Give the position of every Plasmodium parasite.
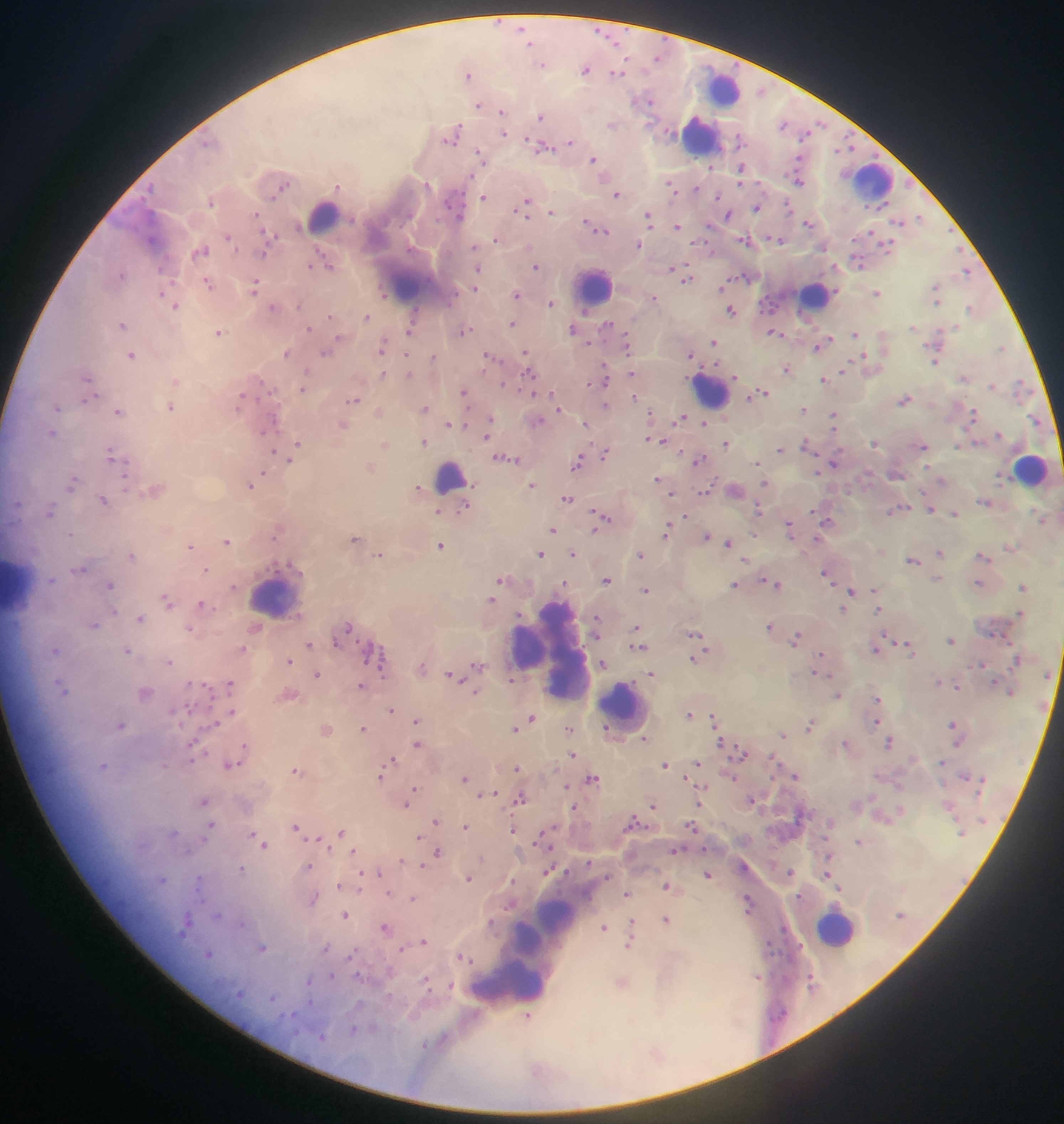
Approximate centers as {x, y} in pixels.
Plasmodium parasites: {497, 21}, {522, 28}, {598, 30}, {608, 36}, {531, 45}, {618, 45}, {625, 59}, {543, 65}, {585, 72}, {613, 73}, {624, 73}, {467, 75}, {650, 103}, {477, 105}, {500, 111}, {541, 118}, {821, 122}, {460, 124}, {784, 126}, {667, 130}, {506, 134}, {739, 134}, {459, 135}, {805, 135}, {526, 139}, {445, 140}, {570, 140}, {542, 141}, {455, 144}, {852, 148}, {551, 149}, {738, 149}, {836, 151}, {479, 152}, {536, 152}, {696, 157}, {798, 157}, {594, 159}, {486, 164}, {740, 164}, {710, 168}, {472, 175}, {668, 182}, {799, 182}, {427, 184}, {741, 184}, {290, 185}, {698, 189}, {281, 190}, {464, 192}, {676, 193}, {618, 195}, {274, 198}, {483, 198}, {445, 201}, {718, 201}, {789, 201}, {527, 202}, {465, 205}, {211, 206}, {449, 207}, {755, 209}, {516, 210}, {552, 211}, {791, 211}, {648, 212}, {257, 214}, {728, 216}, {459, 217}, {528, 217}, {438, 218}, {586, 220}, {810, 224}, {710, 225}, {651, 227}, {678, 228}, {263, 230}, {871, 230}, {595, 232}, {607, 232}, {276, 235}, {749, 236}, {768, 236}, {228, 237}, {740, 238}, {781, 241}, {707, 242}, {881, 242}, {693, 243}, {268, 244}, {495, 244}, {641, 245}, {748, 246}, {473, 247}, {236, 249}, {319, 249}, {854, 254}, {265, 256}, {310, 266}, {535, 266}, {686, 266}, {860, 266}, {157, 269}, {672, 269}, {477, 270}, {965, 272}, {121, 274}, {748, 276}, {731, 278}, {691, 279}, {207, 280}, {257, 280}, {683, 282}, {172, 284}, {721, 288}, {935, 288}, {474, 289}, {209, 290}, {837, 290}, {160, 292}, {878, 292}, {254, 293}, {456, 295}, {385, 296}, {516, 296}, {655, 296}, {760, 301}, {552, 303}, {937, 304}, {174, 307}, {969, 307}, {414, 308}, {730, 308}, {771, 312}, {761, 313}, {329, 316}, {369, 316}, {513, 322}, {415, 323}, {608, 323}, {122, 325}, {309, 327}, {911, 329}, {472, 330}, {407, 331}, {573, 331}, {772, 332}, {216, 333}, {856, 333}, {462, 334}, {624, 334}, {782, 335}, {338, 337}, {830, 338}, {607, 341}, {713, 343}, {591, 344}, {626, 345}, {816, 348}, {381, 352}, {527, 352}, {321, 353}, {485, 353}, {132, 354}, {406, 354}, {690, 354}, {435, 355}, {628, 355}, {863, 356}, {502, 361}, {851, 361}, {935, 361}, {603, 364}, {716, 364}, {701, 366}, {484, 370}, {528, 370}, {786, 371}, {632, 372}, {841, 372}, {383, 374}, {735, 376}, {607, 377}, {86, 379}, {688, 379}, {821, 379}, {503, 382}, {262, 383}, {589, 385}, {607, 385}, {992, 388}, {301, 390}, {464, 390}, {520, 390}, {551, 391}, {763, 391}, {271, 392}, {534, 394}, {634, 395}, {99, 396}, {243, 397}, {749, 397}, {357, 400}, {904, 400}, {82, 401}, {347, 401}, {605, 404}, {236, 407}, {467, 407}, {172, 408}, {558, 408}, {801, 408}, {58, 410}, {973, 410}, {650, 412}, {116, 413}, {832, 415}, {684, 417}, {542, 419}, {492, 420}, {972, 421}, {273, 422}, {675, 423}, {702, 423}, {585, 424}, {449, 425}, {465, 426}, {261, 432}, {277, 432}, {51, 435}, {487, 437}, {806, 438}, {649, 440}, {663, 441}, {426, 443}, {592, 443}, {974, 443}, {296, 444}, {725, 444}, {872, 445}, {923, 447}, {958, 447}, {110, 449}, {606, 449}, {274, 451}, {680, 451}, {779, 452}, {494, 455}, {580, 455}, {704, 457}, {602, 458}, {111, 459}, {288, 460}, {510, 460}, {694, 463}, {758, 464}, {835, 465}, {579, 467}, {263, 471}, {818, 472}, {715, 476}, {123, 477}, {75, 478}, {657, 479}, {764, 482}, {710, 484}, {250, 485}, {531, 486}, {72, 487}, {925, 490}, {709, 492}, {699, 493}, {672, 494}, {566, 499}, {103, 502}, {755, 502}, {469, 506}, {907, 507}, {889, 509}, {591, 510}, {930, 510}, {956, 512}, {811, 513}, {50, 515}, {604, 515}, {686, 517}, {611, 521}, {824, 522}, {668, 523}, {789, 523}, {554, 531}, {595, 531}, {72, 535}, {665, 536}, {707, 536}, {272, 537}, {816, 539}, {228, 542}, {728, 543}, {190, 547}, {538, 552}, {381, 553}, {942, 554}, {978, 554}, {133, 556}, {571, 556}, {743, 560}, {914, 562}, {206, 570}, {278, 571}, {825, 574}, {607, 579}, {762, 580}, {564, 583}, {734, 584}, {980, 584}, {109, 585}, {780, 585}, {832, 585}, {233, 586}, {648, 590}, {851, 592}, {873, 593}, {164, 597}, {201, 603}, {878, 611}, {113, 613}, {139, 618}, {596, 618}, {769, 625}, {638, 626}, {94, 627}, {190, 628}, {349, 628}, {884, 633}, {798, 634}, {695, 636}, {336, 641}, {357, 641}, {894, 641}, {950, 641}, {309, 644}, {794, 644}, {906, 644}, {380, 646}, {636, 646}, {56, 651}, {126, 651}, {708, 651}, {820, 654}, {166, 661}, {290, 662}, {693, 662}, {367, 663}, {601, 663}, {474, 664}, {380, 666}, {319, 673}, {448, 673}, {650, 673}, {814, 673}, {382, 677}, {463, 680}, {512, 680}, {633, 681}, {59, 682}, {203, 683}, {230, 683}, {190, 684}, {362, 686}, {68, 687}, {955, 687}, {476, 692}, {839, 697}, {213, 698}, {879, 698}, {187, 705}, {196, 705}, {392, 709}, {233, 711}, {172, 712}, {711, 714}, {691, 715}, {530, 717}, {418, 721}, {876, 721}, {216, 722}, {952, 724}, {181, 725}, {808, 727}, {363, 728}, {515, 728}, {607, 728}, {783, 735}, {644, 739}, {720, 739}, {197, 740}, {889, 743}, {417, 744}, {190, 745}, {244, 746}, {956, 746}, {205, 752}, {742, 752}, {770, 755}, {392, 759}, {192, 760}, {239, 764}, {664, 764}, {699, 765}, {102, 766}, {384, 766}, {517, 769}, {296, 770}, {596, 776}, {382, 777}, {774, 777}, {688, 778}, {466, 779}, {702, 786}, {566, 787}, {414, 788}, {479, 796}, {517, 798}, {752, 799}, {205, 803}, {406, 805}, {701, 806}, {576, 808}, {651, 808}, {436, 822}, {690, 823}, {210, 824}, {467, 825}, {631, 825}, {297, 828}, {512, 830}, {342, 832}, {253, 833}, {541, 833}, {420, 837}, {318, 838}, {306, 840}, {265, 845}, {330, 848}, {673, 849}, {703, 849}, {355, 851}, {437, 853}, {402, 860}, {589, 863}, {422, 864}, {309, 865}, {241, 867}, {380, 871}, {361, 872}, {545, 872}, {826, 873}, {789, 874}, {707, 875}, {199, 876}, {163, 879}, {469, 879}, {513, 881}, {662, 885}, {339, 886}, {197, 889}, {359, 890}, {389, 893}, {628, 894}, {748, 897}, {800, 899}, {413, 900}, {205, 901}, {505, 908}, {187, 912}, {750, 913}, {219, 915}, {346, 915}, {632, 919}, {667, 920}, {491, 923}, {243, 924}, {383, 927}, {602, 929}, {181, 934}, {424, 943}, {264, 948}, {356, 948}, {325, 950}, {401, 950}, {208, 953}, {459, 956}, {349, 957}, {471, 961}, {357, 974}, {331, 975}, {427, 977}, {308, 981}, {451, 984}, {431, 992}, {273, 999}, {311, 1000}, {293, 1014}, {528, 1016}.

Thick blood film. Image is 1064×1124 pixels. One field of view. Mobile-phone photograph taken through the microscope. Sample from Ghana.